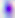

identification = Toxoplasma gondii
modality = photomicrograph
magnification = 400x